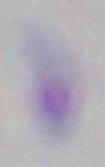
Summary:
  - Magnification: 1000x
  - Identification: Toxoplasma gondii
  - Modality: photomicrograph